Name the parasite shown.
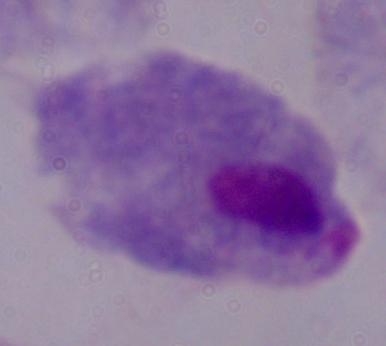

This is a trichomonad.

Captured at 1000x magnification. Micrograph.